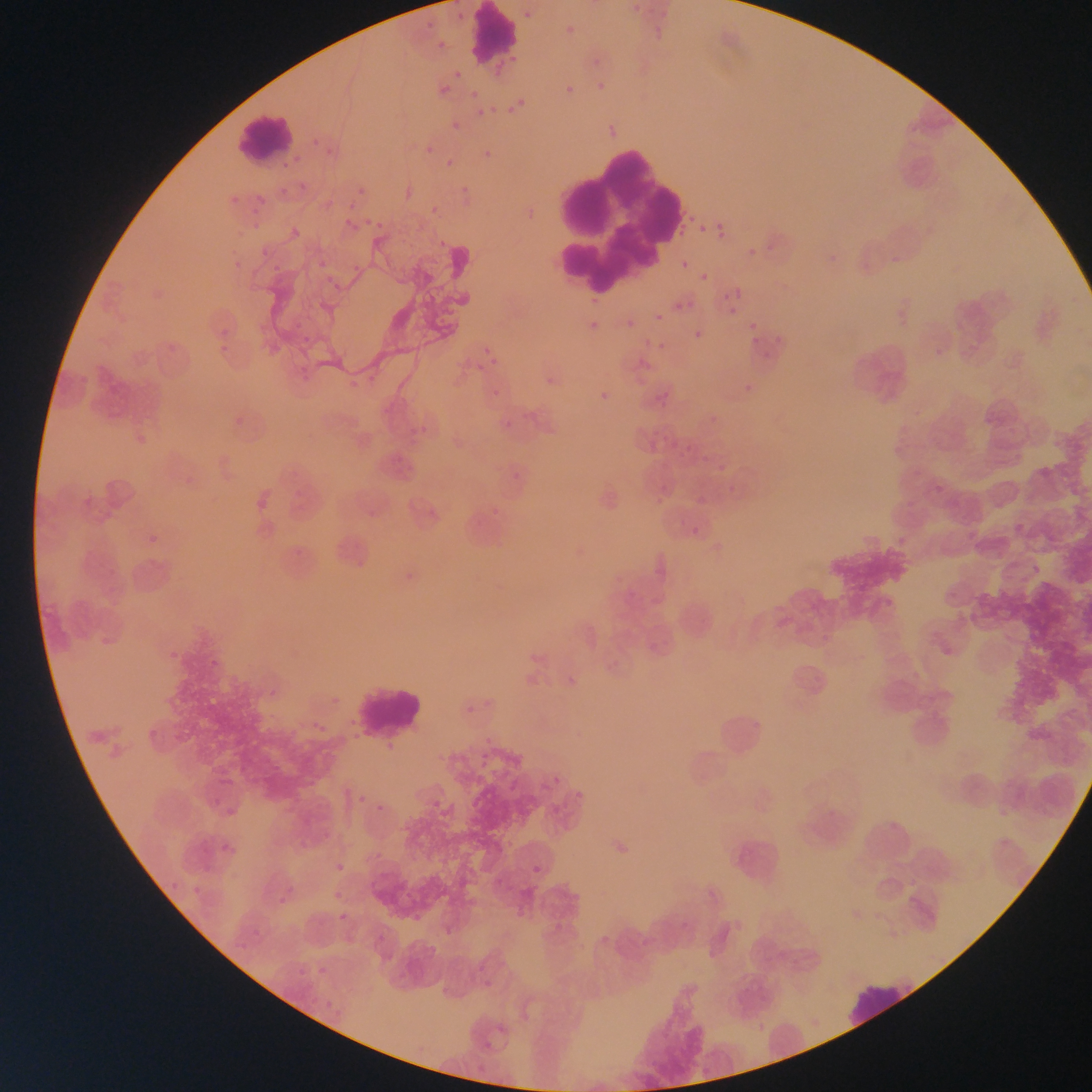 Approximate bounding boxes as {left, top, right, bottom} in pixels. Malaria parasite locations (subset; some below the resolvable size): {632, 5, 640, 13}, {453, 9, 466, 26}, {524, 10, 532, 20}, {645, 10, 672, 36}, {416, 13, 438, 27}, {561, 23, 581, 41}, {429, 41, 447, 54}, {585, 48, 606, 70}, {445, 66, 476, 86}, {594, 81, 609, 90}, {562, 83, 576, 99}, {432, 86, 446, 101}, {511, 94, 533, 114}, {490, 105, 498, 113}, {476, 108, 484, 117}, {606, 112, 619, 142}, {449, 122, 467, 133}, {308, 128, 326, 151}, {417, 132, 443, 160}, {322, 142, 341, 161}, {441, 159, 454, 177}, {393, 174, 418, 198}, {348, 178, 366, 198}, {296, 185, 305, 188}, {277, 186, 295, 200}, {455, 186, 473, 199}, {225, 192, 242, 209}, {250, 200, 268, 209}, {420, 202, 438, 216}, {523, 206, 537, 222}, {364, 213, 387, 234}, {715, 218, 729, 244}, {284, 219, 313, 246}, {344, 219, 352, 227}, {699, 224, 707, 231}, {432, 241, 449, 252}, {255, 247, 268, 257}, {748, 248, 756, 257}, {232, 256, 244, 268}, {681, 260, 690, 269}, {700, 273, 708, 282}, {735, 288, 743, 297}, {723, 292, 731, 301}, {584, 293, 601, 308}, {688, 301, 696, 308}, {673, 303, 682, 311}, {728, 307, 737, 315}, {655, 313, 664, 322}, {585, 319, 601, 335}, {626, 321, 635, 333}, {214, 322, 233, 340}, {749, 322, 757, 330}, {694, 330, 702, 339}, {476, 332, 497, 363}, {751, 336, 760, 344}, {645, 339, 662, 355}, {164, 342, 179, 359}, {735, 371, 754, 392}, {552, 372, 569, 388}, {492, 388, 500, 397}, {593, 390, 612, 404}, {494, 392, 523, 430}, {226, 414, 248, 429}, {401, 422, 438, 441}, {127, 425, 153, 447}, {647, 427, 658, 451}, {711, 457, 728, 479}, {393, 462, 419, 479}, {513, 471, 521, 479}, {723, 473, 742, 499}, {688, 489, 705, 511}, {250, 494, 273, 516}, {420, 508, 445, 522}, {368, 510, 377, 519}, {678, 521, 697, 539}, {144, 523, 165, 541}, {648, 558, 674, 583}, {399, 566, 411, 578}, {167, 645, 180, 662}, {205, 654, 220, 670}, {464, 701, 481, 719}, {304, 718, 328, 733}, {146, 725, 160, 746}, {566, 786, 585, 798}, {202, 787, 221, 811}, {350, 793, 371, 805}, {374, 805, 386, 814}, {214, 837, 234, 855}, {195, 842, 230, 881}, {532, 857, 548, 884}, {330, 862, 344, 877}, {162, 874, 185, 891}, {275, 877, 296, 906}, {188, 878, 209, 902}, {327, 881, 352, 900}, {340, 913, 348, 921}, {681, 920, 690, 930}, {473, 956, 500, 990}, {292, 959, 317, 984}, {309, 966, 331, 990}, {496, 1024, 506, 1034}, {483, 1041, 492, 1050} | approximate {x, y} pixel centers of objects too small to bound: {306, 339}. Leukocyte locations: {469, 5, 519, 65}, {234, 110, 298, 164}, {550, 145, 689, 279}, {350, 681, 428, 743}, {845, 980, 918, 1025}. Thin blood smear. Collected in Ghana. Photographed through a microscope with a mobile-phone camera. Single field of view. Image is 1092×1092 pixels.